Comment on the background quality.
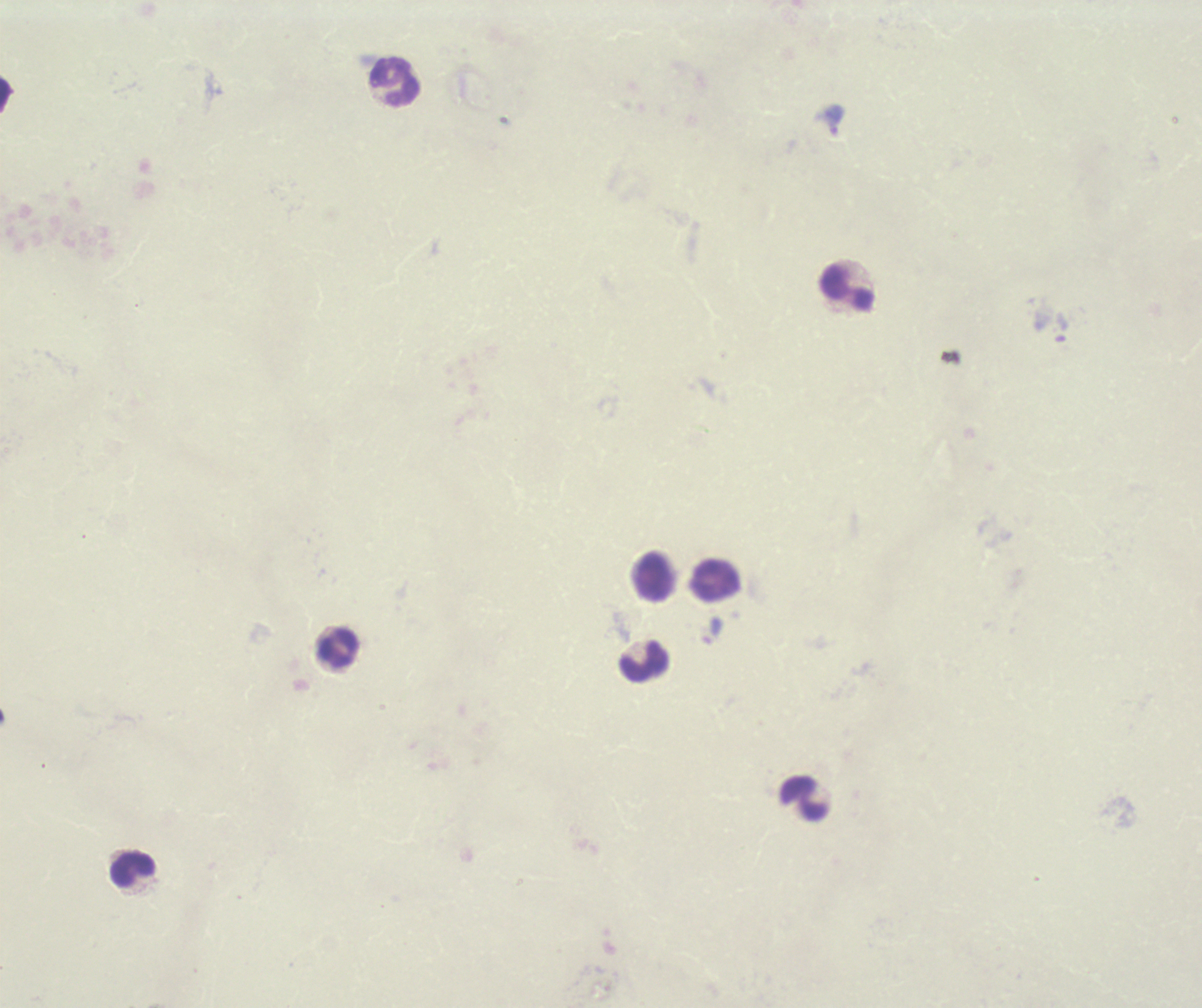
Unsatisfactory.

Approximate centers as {x, y} in pixels. Leukocyte locations: {395, 82}, {848, 289}, {655, 577}, {717, 580}, {338, 649}, {644, 663}, {805, 798}, {132, 869}. Thick smear of blood. Image is 1202×1008 pixels. Romanowsky-stained preparation. Previously used in a real diagnosis. 100x magnification. Result: negative for Plasmodium parasites. Single field of view.